Assess this cell for malaria.
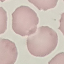

Uninfected.

Photographed with a smartphone camera at the microscope eyepiece. Giemsa stain. Cell patch, automatically extracted from a larger field of view and resized to 64 × 64 pixels. Thin blood smear.